State the blood parasite species.
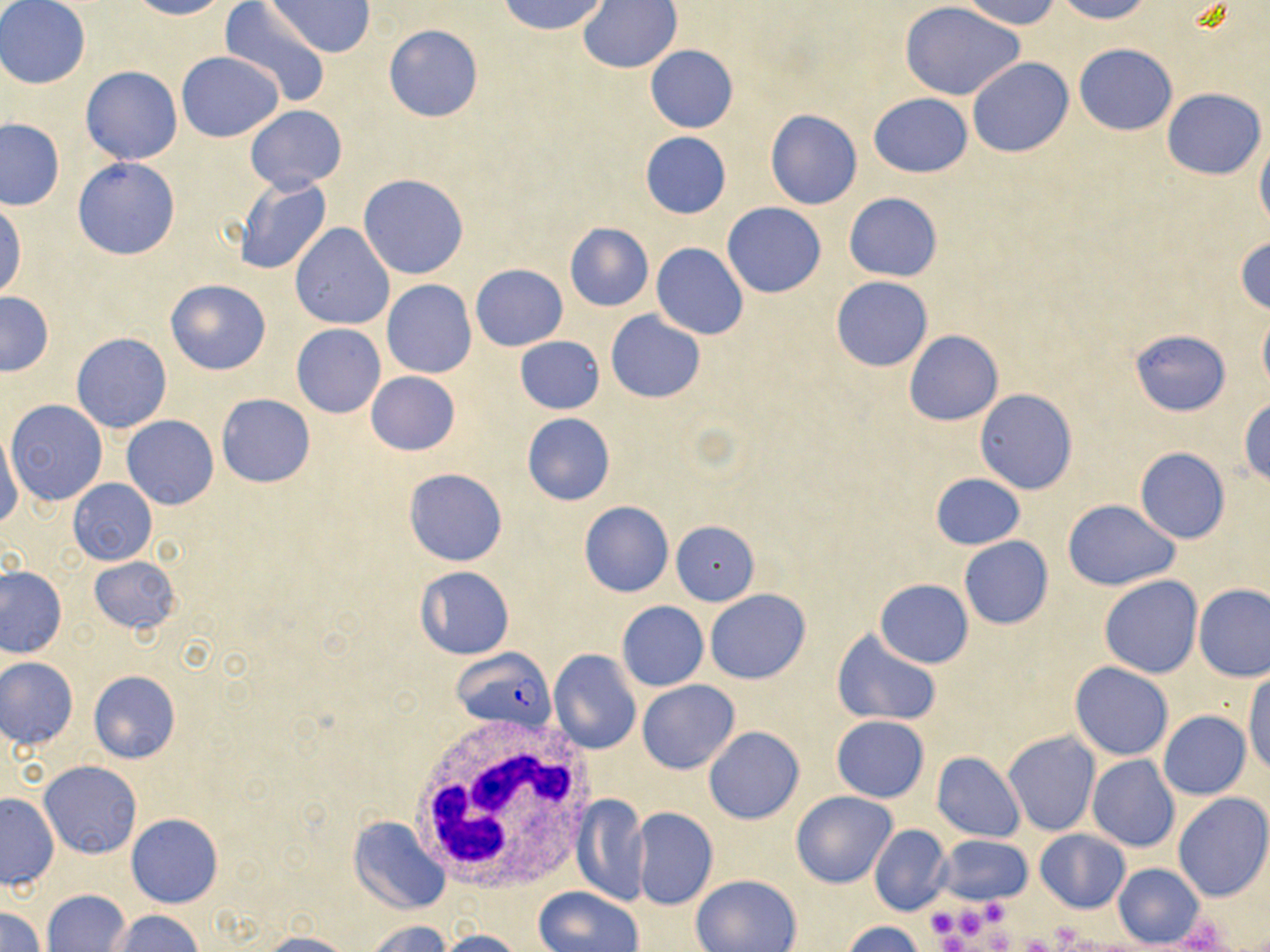

Plasmodium falciparum.

Summary:
  - Coordinate format: approximate bounding boxes as [x1, y1, x2, y2] in pixels
  - White blood cell locations: [404, 712, 600, 896]
  - Uninfected red blood cell locations: [126, 0, 234, 20], [498, 0, 612, 36], [960, 0, 1063, 27], [1053, 0, 1155, 23], [0, 1, 90, 89], [265, 1, 375, 58], [577, 1, 682, 73], [219, 2, 331, 108], [901, 2, 1024, 101], [383, 24, 483, 123], [644, 44, 737, 134], [1074, 44, 1177, 135], [176, 51, 284, 142], [967, 57, 1073, 157], [81, 66, 182, 165], [1163, 87, 1265, 180], [868, 93, 974, 178], [245, 105, 347, 193], [765, 110, 862, 209], [0, 118, 65, 210], [640, 133, 730, 218], [1254, 134, 1270, 235], [73, 158, 180, 261], [358, 173, 470, 280], [234, 177, 332, 277], [844, 193, 942, 282], [0, 197, 26, 300], [723, 203, 826, 297], [563, 223, 654, 312], [290, 224, 393, 330], [1234, 236, 1270, 315], [652, 243, 748, 339], [471, 263, 568, 350], [831, 276, 933, 371], [164, 278, 272, 376], [382, 280, 476, 378], [0, 292, 54, 377], [1258, 307, 1270, 394], [605, 310, 705, 403], [292, 323, 385, 417], [1130, 329, 1231, 416], [903, 330, 1003, 426], [71, 332, 173, 433], [514, 336, 605, 415], [365, 372, 460, 455], [975, 390, 1077, 494], [216, 394, 315, 487], [1239, 397, 1270, 485], [6, 399, 107, 506], [522, 413, 615, 505], [121, 415, 219, 510], [0, 433, 23, 532], [1134, 448, 1230, 543], [403, 468, 507, 567], [930, 472, 1026, 550], [68, 479, 157, 564], [1063, 499, 1180, 590], [579, 500, 673, 597], [671, 520, 760, 605], [959, 536, 1053, 630], [88, 555, 182, 636], [1, 565, 67, 657], [414, 566, 514, 660], [1099, 575, 1202, 678], [876, 579, 973, 668], [1194, 583, 1270, 681], [705, 589, 812, 685], [617, 601, 708, 690], [831, 628, 942, 727], [549, 650, 641, 755], [1, 657, 79, 749], [1070, 662, 1173, 760], [88, 671, 180, 763], [1244, 672, 1270, 776], [637, 680, 740, 774], [1159, 711, 1250, 800], [831, 715, 929, 802], [703, 726, 805, 823], [1003, 731, 1100, 836], [932, 751, 1025, 842], [1088, 756, 1179, 852], [39, 760, 142, 859], [791, 791, 897, 889], [1172, 793, 1270, 902], [0, 794, 59, 890], [573, 794, 647, 905], [632, 808, 718, 911], [127, 813, 223, 908], [349, 817, 450, 914], [869, 824, 952, 916], [1035, 830, 1130, 913], [936, 835, 1032, 906], [1113, 864, 1205, 947], [693, 875, 801, 952], [535, 887, 642, 952], [42, 889, 133, 952], [1, 908, 46, 952], [112, 909, 203, 951], [363, 920, 453, 952], [841, 921, 930, 952], [438, 928, 525, 952], [260, 932, 353, 952]
  - Plasmodium falciparum-infected red blood cell locations: [452, 647, 555, 731]
  - Platelet locations: [977, 894, 1012, 929], [924, 905, 961, 942], [960, 909, 985, 938], [1185, 921, 1224, 952], [1057, 925, 1084, 946], [990, 930, 1013, 952], [944, 934, 966, 952], [1021, 936, 1054, 952]
  - Modality: light microscopy
  - Stain: May-Grünwald-Giemsa
  - Magnification: 1000x
  - Field of view: one of a larger specimen
  - Image size: 1270×952 pixels
  - Preparation: thin blood smear